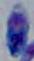

Summary:
  - Magnification: 1000x
  - Modality: micrograph
  - Identification: Toxoplasma gondii